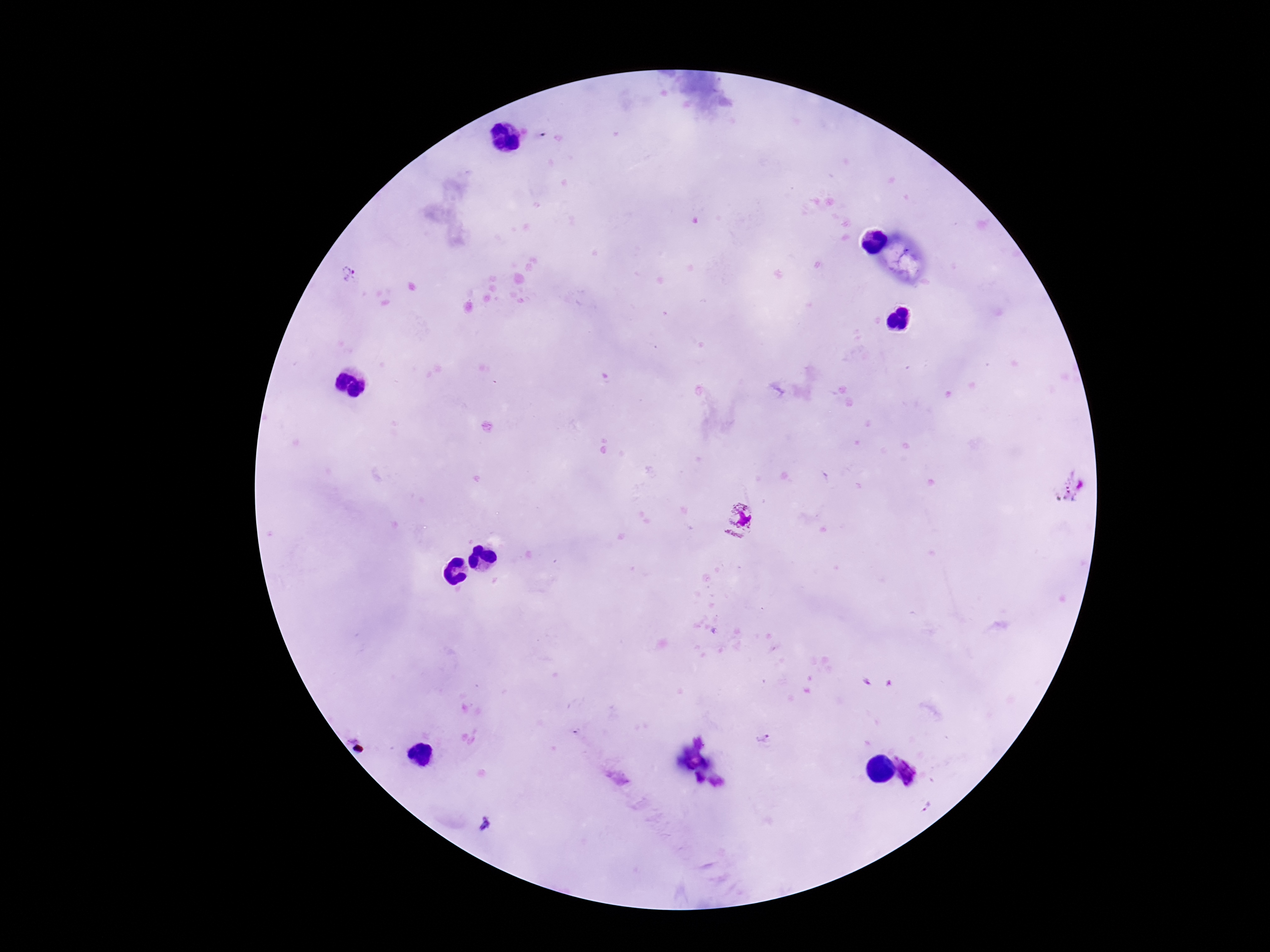

Approximate centers as [x, y] in pixels. Plasmodium parasite locations: [350, 275], [740, 519], [764, 738], [912, 766]. Photographed through the microscope eyepiece with a smartphone camera. Thick blood smear. Image is 1270×952 pixels. One field from this slide. 100x magnification. Giemsa-stained preparation. Patient malaria status: infected.